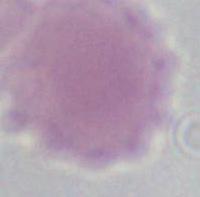

1000x magnification. An erythrocyte is shown. Micrograph.